Report the malaria status.
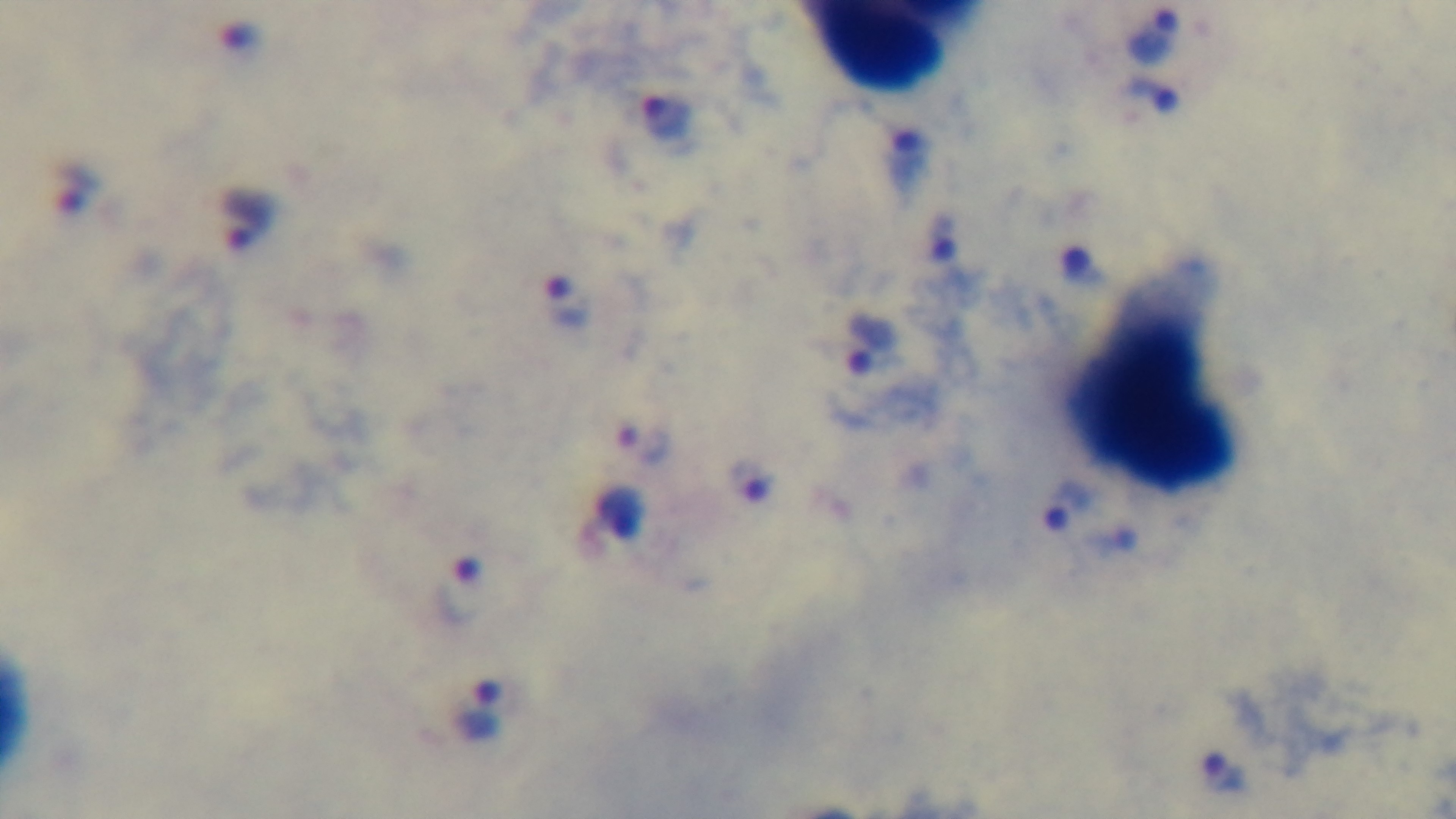
Positive.

Summary:
  - Field of view: one from the slide
  - Objective: 100x oil immersion
  - Capture: mounted 4K digital camera
  - Stain: Giemsa
  - Preparation: thick
  - Modality: light microscopy